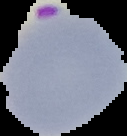

image type = cell region segmented out of the field of view; surrounding area masked to black
malaria status = parasitized
preparation = thin blood film
image size = 127×136 pixels